Locate and identify every blood parasite.
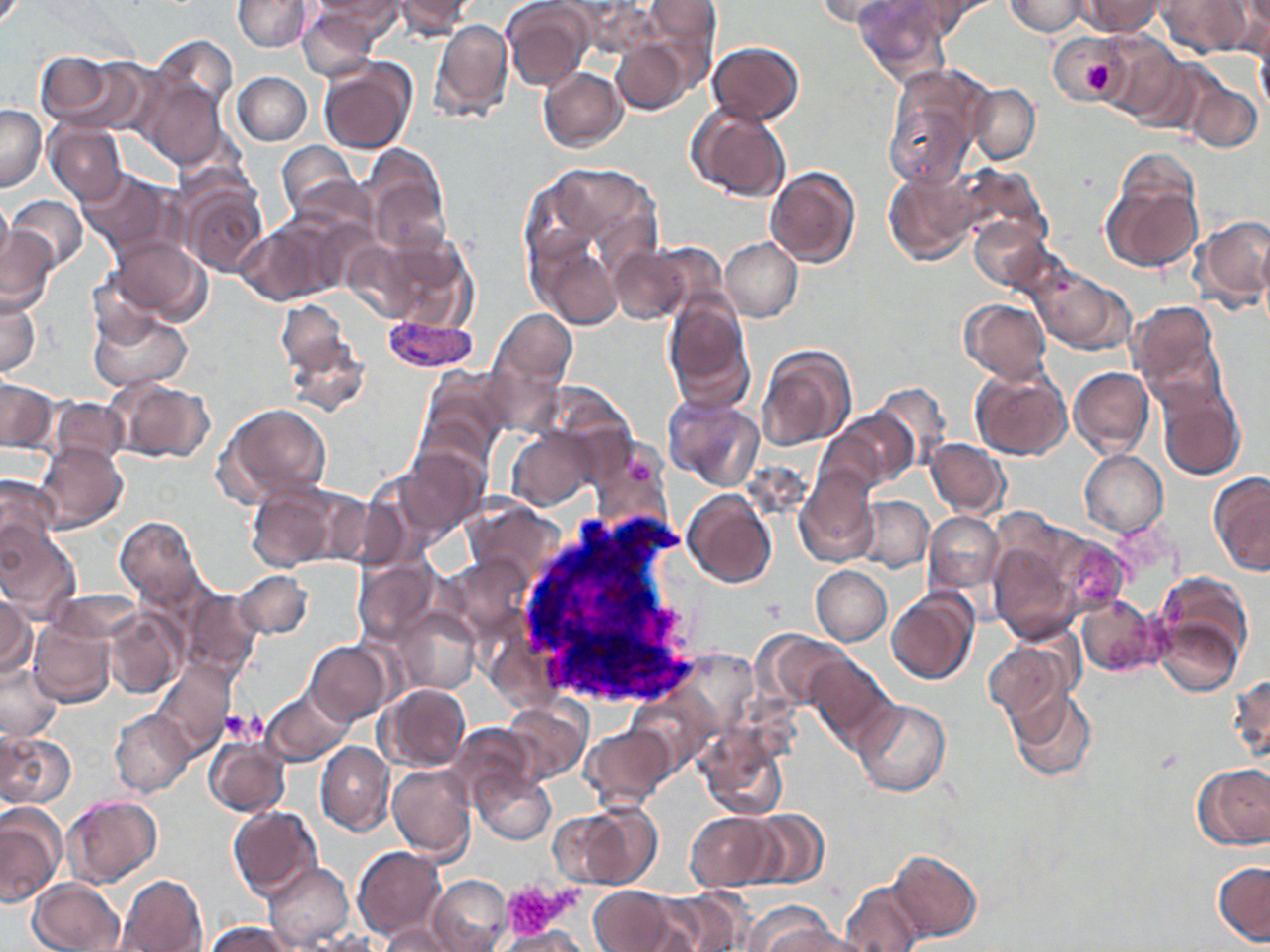

Approximate bounding boxes as named x1/y1/x2/y2 corners in pixels.
Plasmodium vivax-infected red blood cells: (x1=382, y1=315, x2=479, y2=373).
No Plasmodium falciparum, Plasmodium ovale, Plasmodium malariae, Babesia divergens, or Trypanosoma brucei observed.

Platelet locations: (x1=1079, y1=56, x2=1113, y2=101), (x1=223, y1=709, x2=265, y2=744), (x1=502, y1=879, x2=572, y2=938). Uninfected red blood cell locations: (x1=234, y1=0, x2=313, y2=52), (x1=307, y1=0, x2=404, y2=40), (x1=392, y1=0, x2=473, y2=38), (x1=501, y1=0, x2=593, y2=90), (x1=816, y1=0, x2=920, y2=32), (x1=1006, y1=0, x2=1088, y2=36), (x1=1078, y1=0, x2=1164, y2=37), (x1=1158, y1=0, x2=1247, y2=58), (x1=1225, y1=0, x2=1270, y2=59), (x1=236, y1=1, x2=381, y2=63), (x1=639, y1=1, x2=720, y2=76), (x1=855, y1=1, x2=951, y2=82), (x1=296, y1=7, x2=379, y2=81), (x1=430, y1=19, x2=513, y2=124), (x1=1097, y1=31, x2=1187, y2=119), (x1=1049, y1=32, x2=1125, y2=103), (x1=149, y1=36, x2=237, y2=116), (x1=611, y1=38, x2=690, y2=115), (x1=1255, y1=38, x2=1270, y2=119), (x1=708, y1=42, x2=804, y2=124), (x1=34, y1=51, x2=135, y2=130), (x1=318, y1=58, x2=417, y2=154), (x1=538, y1=67, x2=627, y2=151), (x1=233, y1=72, x2=312, y2=145), (x1=134, y1=75, x2=228, y2=171), (x1=881, y1=78, x2=979, y2=189), (x1=1185, y1=81, x2=1262, y2=152), (x1=969, y1=84, x2=1040, y2=164), (x1=687, y1=104, x2=791, y2=202), (x1=0, y1=106, x2=46, y2=192), (x1=45, y1=121, x2=127, y2=204), (x1=277, y1=140, x2=360, y2=218), (x1=360, y1=145, x2=448, y2=249), (x1=953, y1=164, x2=1046, y2=249), (x1=522, y1=165, x2=660, y2=315), (x1=765, y1=167, x2=860, y2=267), (x1=77, y1=169, x2=174, y2=257), (x1=884, y1=169, x2=978, y2=265), (x1=1101, y1=170, x2=1203, y2=275), (x1=178, y1=180, x2=268, y2=278), (x1=0, y1=193, x2=12, y2=272), (x1=8, y1=195, x2=87, y2=272), (x1=1189, y1=215, x2=1270, y2=311), (x1=971, y1=217, x2=1055, y2=291), (x1=238, y1=220, x2=344, y2=305), (x1=364, y1=228, x2=475, y2=331), (x1=0, y1=229, x2=58, y2=314), (x1=1256, y1=229, x2=1270, y2=328), (x1=339, y1=237, x2=428, y2=324), (x1=720, y1=237, x2=803, y2=322), (x1=110, y1=238, x2=211, y2=325), (x1=538, y1=242, x2=622, y2=328), (x1=610, y1=246, x2=695, y2=323), (x1=1029, y1=267, x2=1133, y2=355), (x1=0, y1=295, x2=41, y2=378), (x1=663, y1=297, x2=753, y2=409), (x1=960, y1=299, x2=1051, y2=384), (x1=277, y1=300, x2=350, y2=375), (x1=1130, y1=302, x2=1225, y2=408), (x1=88, y1=307, x2=192, y2=392), (x1=491, y1=309, x2=577, y2=391), (x1=280, y1=324, x2=371, y2=416), (x1=755, y1=345, x2=855, y2=451), (x1=1069, y1=366, x2=1154, y2=458), (x1=418, y1=369, x2=513, y2=464), (x1=972, y1=369, x2=1071, y2=462), (x1=108, y1=377, x2=216, y2=464), (x1=0, y1=379, x2=57, y2=453), (x1=1157, y1=379, x2=1245, y2=480), (x1=869, y1=383, x2=952, y2=468), (x1=47, y1=396, x2=127, y2=465), (x1=664, y1=396, x2=763, y2=490), (x1=220, y1=403, x2=333, y2=505), (x1=832, y1=408, x2=917, y2=489), (x1=507, y1=428, x2=598, y2=510), (x1=926, y1=438, x2=1009, y2=518), (x1=35, y1=441, x2=127, y2=534), (x1=398, y1=446, x2=488, y2=539), (x1=1080, y1=450, x2=1168, y2=538), (x1=795, y1=467, x2=878, y2=565), (x1=1209, y1=472, x2=1270, y2=576), (x1=0, y1=475, x2=62, y2=563), (x1=245, y1=481, x2=345, y2=572), (x1=682, y1=489, x2=778, y2=588), (x1=857, y1=497, x2=934, y2=573), (x1=463, y1=499, x2=564, y2=585), (x1=923, y1=511, x2=1003, y2=593), (x1=116, y1=516, x2=205, y2=609), (x1=0, y1=524, x2=82, y2=623), (x1=1052, y1=535, x2=1130, y2=613), (x1=988, y1=542, x2=1082, y2=643), (x1=446, y1=554, x2=536, y2=643), (x1=354, y1=558, x2=440, y2=643), (x1=811, y1=566, x2=892, y2=645), (x1=233, y1=571, x2=313, y2=640), (x1=1150, y1=572, x2=1253, y2=689), (x1=179, y1=587, x2=261, y2=681), (x1=886, y1=589, x2=978, y2=686), (x1=45, y1=590, x2=144, y2=646), (x1=0, y1=594, x2=34, y2=679), (x1=1076, y1=596, x2=1159, y2=676), (x1=395, y1=607, x2=481, y2=694), (x1=103, y1=608, x2=184, y2=698), (x1=28, y1=617, x2=116, y2=708), (x1=758, y1=631, x2=851, y2=710), (x1=983, y1=638, x2=1073, y2=723), (x1=306, y1=641, x2=393, y2=724), (x1=806, y1=656, x2=895, y2=749), (x1=0, y1=663, x2=61, y2=740), (x1=152, y1=664, x2=235, y2=754), (x1=1228, y1=674, x2=1269, y2=771), (x1=380, y1=684, x2=470, y2=772), (x1=262, y1=688, x2=352, y2=766), (x1=1006, y1=688, x2=1096, y2=782), (x1=503, y1=698, x2=592, y2=783), (x1=851, y1=699, x2=951, y2=797), (x1=109, y1=710, x2=194, y2=797), (x1=448, y1=723, x2=541, y2=805), (x1=582, y1=725, x2=675, y2=807), (x1=695, y1=728, x2=789, y2=823), (x1=0, y1=731, x2=74, y2=809), (x1=204, y1=736, x2=289, y2=816), (x1=315, y1=742, x2=394, y2=835), (x1=387, y1=763, x2=476, y2=862), (x1=1194, y1=763, x2=1270, y2=850), (x1=471, y1=768, x2=556, y2=846), (x1=64, y1=795, x2=161, y2=887), (x1=561, y1=802, x2=661, y2=890), (x1=0, y1=805, x2=65, y2=906), (x1=228, y1=805, x2=322, y2=901), (x1=747, y1=809, x2=829, y2=888), (x1=685, y1=811, x2=780, y2=892), (x1=352, y1=846, x2=447, y2=938), (x1=887, y1=849, x2=981, y2=941), (x1=264, y1=857, x2=442, y2=942), (x1=1213, y1=860, x2=1270, y2=947), (x1=264, y1=863, x2=353, y2=951), (x1=116, y1=875, x2=207, y2=952), (x1=427, y1=875, x2=512, y2=952), (x1=27, y1=878, x2=125, y2=952), (x1=840, y1=880, x2=928, y2=952), (x1=588, y1=885, x2=681, y2=952), (x1=659, y1=889, x2=752, y2=952), (x1=747, y1=905, x2=845, y2=952), (x1=207, y1=921, x2=295, y2=952), (x1=383, y1=922, x2=462, y2=952), (x1=498, y1=925, x2=588, y2=952), (x1=763, y1=926, x2=870, y2=952), (x1=304, y1=931, x2=382, y2=952). Slide-level diagnosis: Plasmodium vivax. May-Grünwald-Giemsa-stained preparation. Optical microscopy. One field of a larger specimen. 1000x magnification. Image is 1270×952 pixels. Thin blood film.